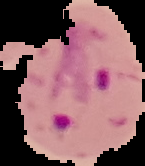

Summary:
  - Image size: 145×166 pixels
  - Result: Plasmodium parasites identified
  - Preparation: thin blood smear
  - Image type: segmented cell region on a black background